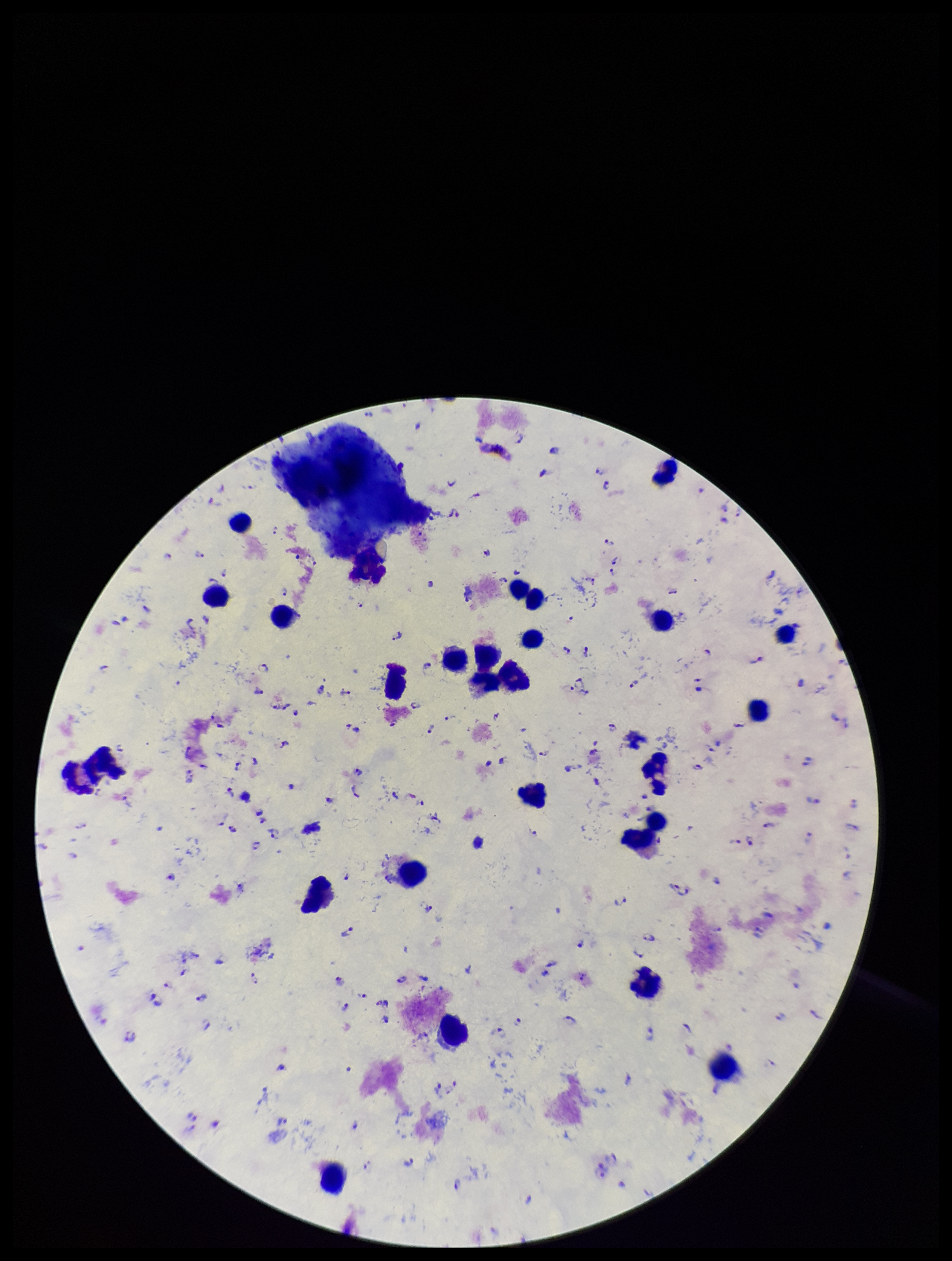

Summary:
  - Plasmodium parasites: seen
  - Field of view: one from this slide
  - Preparation: thick
  - Patient malaria status: positive
  - Parasite count: 120
  - Image size: 952×1261 pixels
  - Species reported for this patient: Plasmodium falciparum
  - Capture: smartphone photograph through the microscope eyepiece
  - Leukocyte count: 27
  - Stain: Giemsa